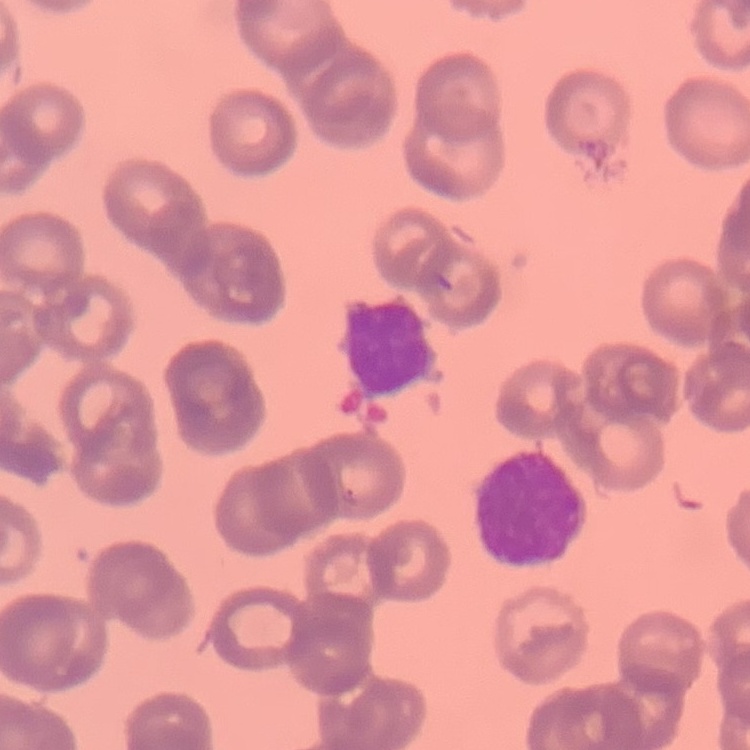
red_blood_cell_morphology: rouleaux formation
preparation: thin blood film
stain: Field's or Giemsa
image_type: one tile cut from a larger photomicrograph